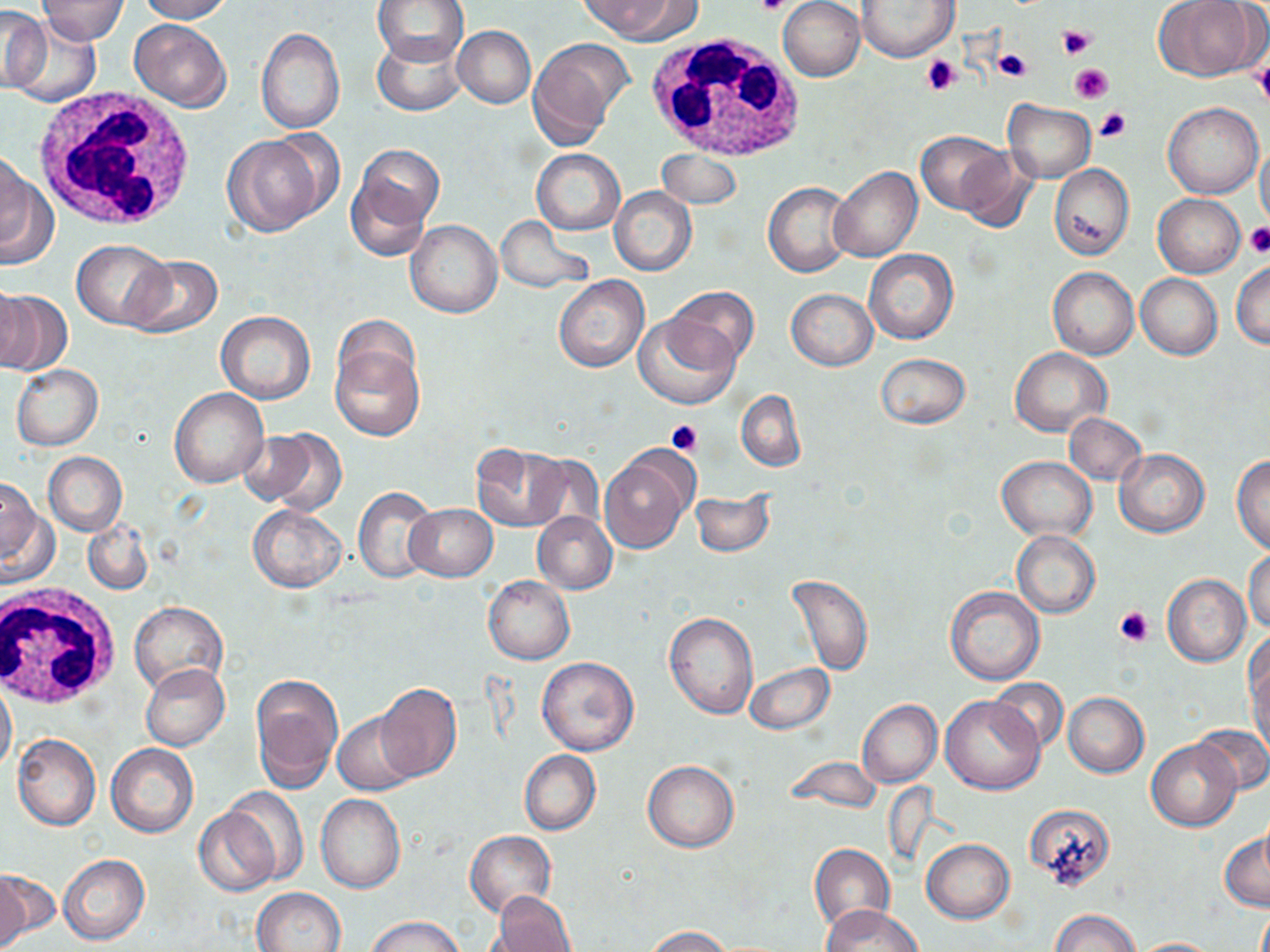

slide-level diagnosis = negative for blood parasites
image size = 1270×952 pixels
stain = May-Grünwald-Giemsa
modality = light microscopy
uninfected red blood cell locations = approximate bounding boxes as (x1, y1, x2, y2) in pixels: (38, 0, 127, 46), (134, 0, 236, 22), (371, 0, 470, 68), (579, 0, 688, 41), (778, 0, 866, 82), (1157, 0, 1261, 82), (856, 1, 959, 63), (1, 6, 50, 94), (10, 18, 103, 106), (130, 19, 232, 111), (452, 25, 535, 107), (256, 28, 345, 134), (371, 35, 466, 117), (528, 39, 628, 146), (1003, 99, 1095, 182), (1163, 103, 1262, 199), (916, 130, 1006, 213), (223, 134, 328, 237), (357, 139, 442, 227), (1256, 141, 1270, 230), (954, 146, 1040, 232), (531, 148, 625, 235), (656, 149, 743, 209), (0, 150, 30, 247), (0, 156, 54, 270), (1049, 164, 1133, 260), (347, 165, 435, 261), (829, 166, 922, 263), (763, 182, 855, 278), (610, 188, 697, 276), (1153, 194, 1245, 277), (493, 216, 595, 293), (405, 219, 502, 317), (71, 241, 172, 328), (864, 248, 958, 345), (123, 255, 222, 339), (1231, 260, 1269, 349), (1047, 267, 1139, 359), (1136, 273, 1222, 360), (553, 275, 649, 372), (0, 280, 30, 371), (664, 286, 758, 370), (0, 288, 70, 377), (786, 288, 877, 371), (216, 310, 315, 405), (634, 315, 739, 410), (330, 336, 425, 442), (1010, 347, 1110, 437), (876, 353, 970, 429), (11, 364, 103, 450), (169, 389, 267, 489), (736, 389, 806, 472), (1064, 413, 1146, 486), (246, 428, 345, 514), (473, 443, 571, 532), (1115, 449, 1208, 537), (600, 450, 693, 553), (43, 452, 127, 535), (1231, 453, 1270, 552), (996, 456, 1095, 540), (1, 476, 50, 578), (353, 487, 436, 583), (690, 490, 773, 557), (246, 504, 346, 593), (405, 504, 498, 582), (532, 511, 617, 593), (82, 520, 153, 596), (1012, 531, 1100, 618), (1245, 549, 1270, 632), (788, 574, 874, 675), (1163, 574, 1249, 667), (483, 576, 574, 665), (944, 586, 1045, 687), (129, 601, 228, 693), (664, 612, 758, 719), (1244, 630, 1270, 717), (537, 656, 640, 756), (1248, 662, 1270, 759), (141, 663, 230, 750), (743, 664, 835, 734), (250, 674, 343, 791), (1, 676, 17, 778), (987, 678, 1068, 754), (373, 683, 462, 781), (1064, 692, 1149, 777), (940, 694, 1044, 794), (858, 699, 942, 788), (333, 712, 421, 796), (1191, 724, 1270, 794), (13, 735, 101, 830), (1148, 740, 1240, 831), (106, 743, 198, 838), (519, 749, 600, 835), (785, 756, 881, 813), (642, 760, 739, 852), (222, 787, 309, 887), (316, 795, 405, 893), (1026, 802, 1115, 887), (194, 805, 282, 897), (1219, 829, 1269, 912), (465, 831, 555, 917), (921, 839, 1015, 923), (809, 843, 896, 933), (57, 854, 149, 945), (0, 869, 31, 951), (253, 887, 346, 951), (492, 893, 577, 952), (820, 904, 923, 951), (1049, 908, 1141, 952), (366, 916, 466, 952), (642, 926, 735, 952), (1128, 937, 1226, 952)
field of view = one of a larger specimen
white blood cell locations = approximate bounding boxes as (x1, y1, x2, y2) in pixels: (642, 32, 811, 166), (32, 88, 197, 235), (2, 585, 120, 709)
preparation = thin blood film
magnification = 1000x
platelet locations = approximate bounding boxes as (x1, y1, x2, y2) in pixels: (757, 0, 792, 16), (1058, 26, 1095, 58), (993, 48, 1032, 83), (921, 54, 964, 95), (1253, 60, 1270, 108), (1070, 64, 1113, 103), (1095, 107, 1131, 142), (1245, 223, 1270, 257), (667, 420, 703, 457), (1115, 606, 1153, 646)